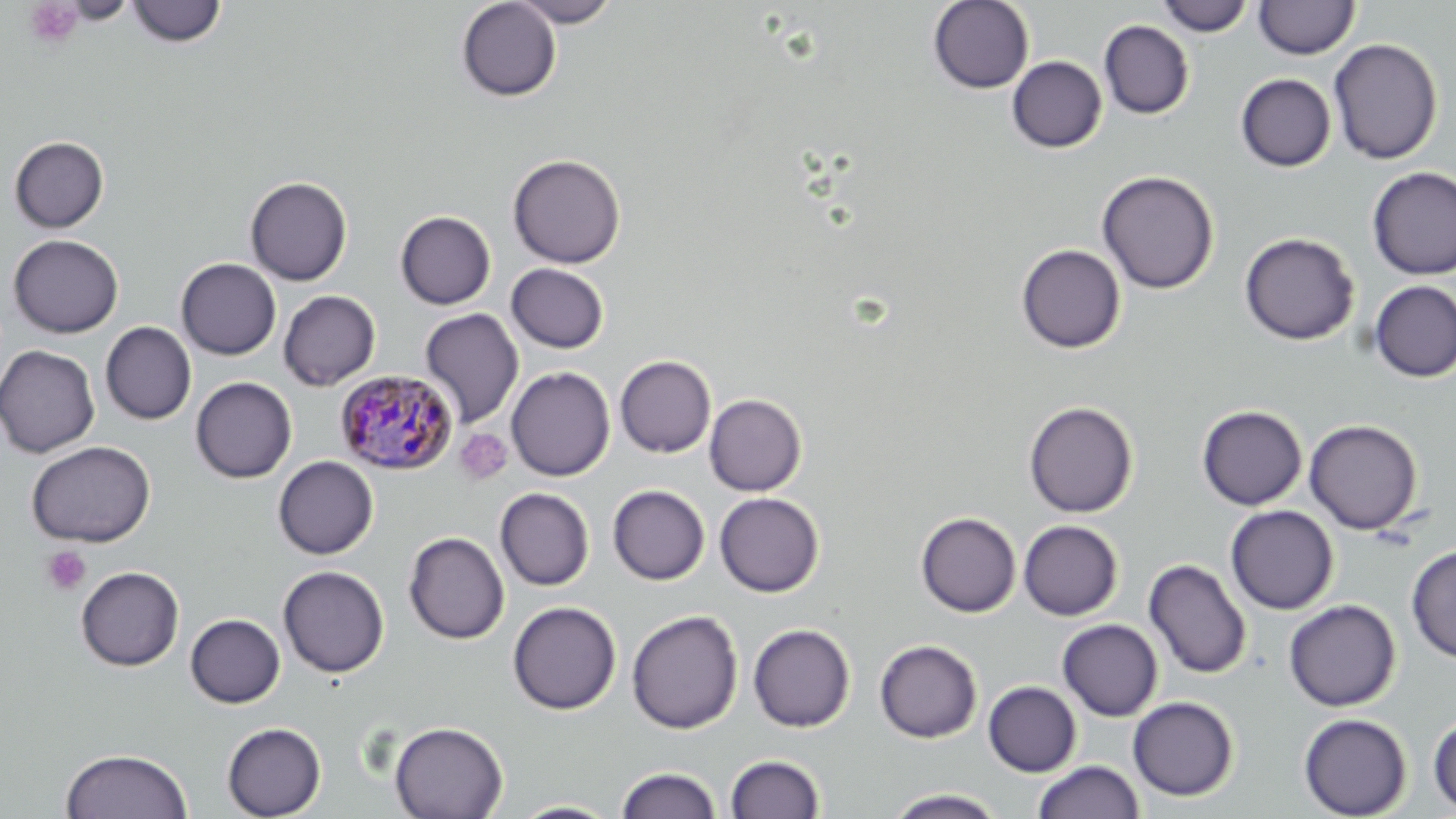 Approximate bounding boxes as named x1/y1/x2/y2 corners in pixels. Uninfected red blood cell locations: (x1=456, y1=0, x2=562, y2=102), (x1=510, y1=0, x2=621, y2=27), (x1=1155, y1=0, x2=1255, y2=36), (x1=1253, y1=0, x2=1359, y2=59), (x1=127, y1=1, x2=227, y2=48), (x1=928, y1=1, x2=1035, y2=94), (x1=1099, y1=20, x2=1195, y2=119), (x1=1328, y1=38, x2=1443, y2=165), (x1=1349, y1=39, x2=1449, y2=275), (x1=1007, y1=56, x2=1107, y2=152), (x1=1236, y1=73, x2=1336, y2=171), (x1=9, y1=136, x2=109, y2=232), (x1=507, y1=153, x2=626, y2=268), (x1=1367, y1=167, x2=1456, y2=280), (x1=1097, y1=170, x2=1219, y2=294), (x1=244, y1=176, x2=352, y2=286), (x1=395, y1=211, x2=496, y2=310), (x1=1239, y1=232, x2=1360, y2=346), (x1=8, y1=234, x2=123, y2=338), (x1=1016, y1=244, x2=1126, y2=353), (x1=176, y1=258, x2=281, y2=360), (x1=506, y1=263, x2=610, y2=354), (x1=1369, y1=280, x2=1456, y2=383), (x1=278, y1=290, x2=381, y2=391), (x1=420, y1=309, x2=524, y2=428), (x1=100, y1=322, x2=197, y2=425), (x1=0, y1=344, x2=100, y2=458), (x1=615, y1=355, x2=716, y2=458), (x1=506, y1=366, x2=615, y2=481), (x1=190, y1=376, x2=297, y2=483), (x1=704, y1=394, x2=807, y2=496), (x1=1023, y1=401, x2=1138, y2=518), (x1=1196, y1=405, x2=1307, y2=510), (x1=1304, y1=419, x2=1423, y2=534), (x1=26, y1=440, x2=155, y2=547), (x1=273, y1=456, x2=378, y2=559), (x1=608, y1=485, x2=710, y2=585), (x1=495, y1=488, x2=595, y2=590), (x1=714, y1=492, x2=824, y2=596), (x1=1226, y1=505, x2=1339, y2=614), (x1=916, y1=512, x2=1021, y2=617), (x1=1018, y1=520, x2=1123, y2=620), (x1=404, y1=532, x2=510, y2=644), (x1=1406, y1=543, x2=1456, y2=664), (x1=1143, y1=559, x2=1252, y2=679), (x1=277, y1=565, x2=389, y2=678), (x1=76, y1=566, x2=184, y2=671), (x1=1283, y1=599, x2=1401, y2=711), (x1=507, y1=601, x2=621, y2=715), (x1=507, y1=604, x2=740, y2=725), (x1=626, y1=609, x2=743, y2=734), (x1=185, y1=614, x2=285, y2=708), (x1=1057, y1=619, x2=1163, y2=721), (x1=748, y1=623, x2=855, y2=732), (x1=874, y1=639, x2=982, y2=743), (x1=983, y1=681, x2=1082, y2=776), (x1=1127, y1=696, x2=1239, y2=801), (x1=1298, y1=713, x2=1412, y2=818), (x1=1428, y1=714, x2=1456, y2=814), (x1=389, y1=721, x2=508, y2=819), (x1=221, y1=722, x2=327, y2=818), (x1=60, y1=748, x2=193, y2=819), (x1=724, y1=753, x2=825, y2=818), (x1=1032, y1=760, x2=1145, y2=819), (x1=616, y1=766, x2=722, y2=819), (x1=885, y1=788, x2=1007, y2=818), (x1=509, y1=800, x2=622, y2=818). Plasmodium malariae-infected red blood cell locations: (x1=334, y1=369, x2=459, y2=475). Platelet locations: (x1=24, y1=1, x2=83, y2=49), (x1=454, y1=428, x2=512, y2=484), (x1=41, y1=546, x2=91, y2=595). Slide-level diagnosis: Plasmodium malariae. Optical microscopy. Thin blood film. Single field of view. Image is 1456×819 pixels. May-Grünwald-Giemsa-stained preparation. 1000x magnification.